Report the malaria status.
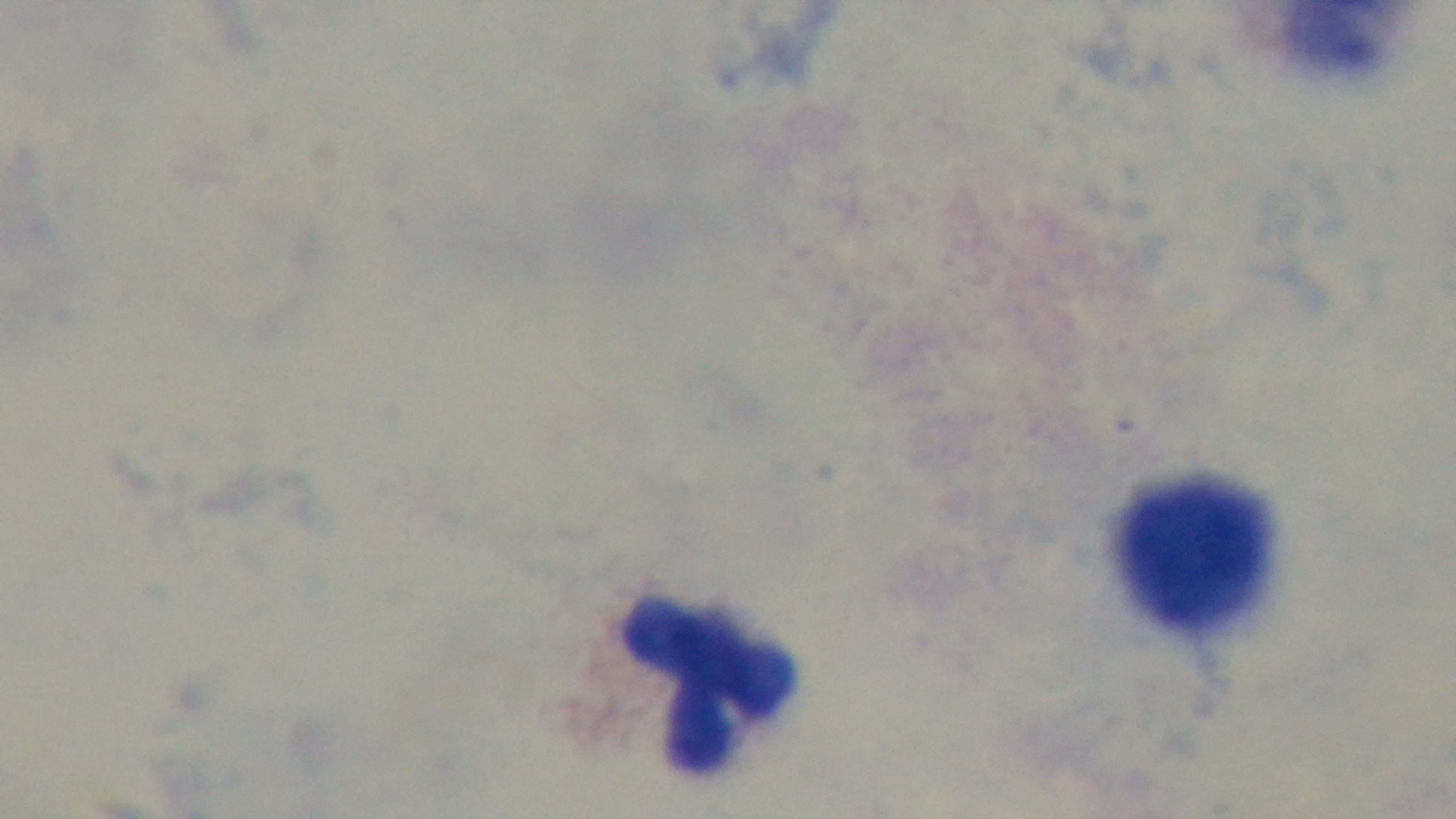

Uninfected.

Single field of view. Photomicrograph. Preparation: thick smear. Captured with a mounted 4K digital camera. Oil-immersion objective, 100x. Giemsa-stained.